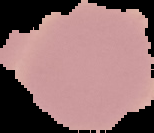
The area outside the segmented cell region is set to black. Image is 154×133 pixels. Result: no Plasmodium parasites seen. From a thin blood film.